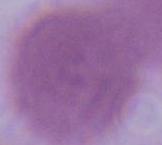 Captured at 1000x magnification. Micrograph. A red blood cell is shown.